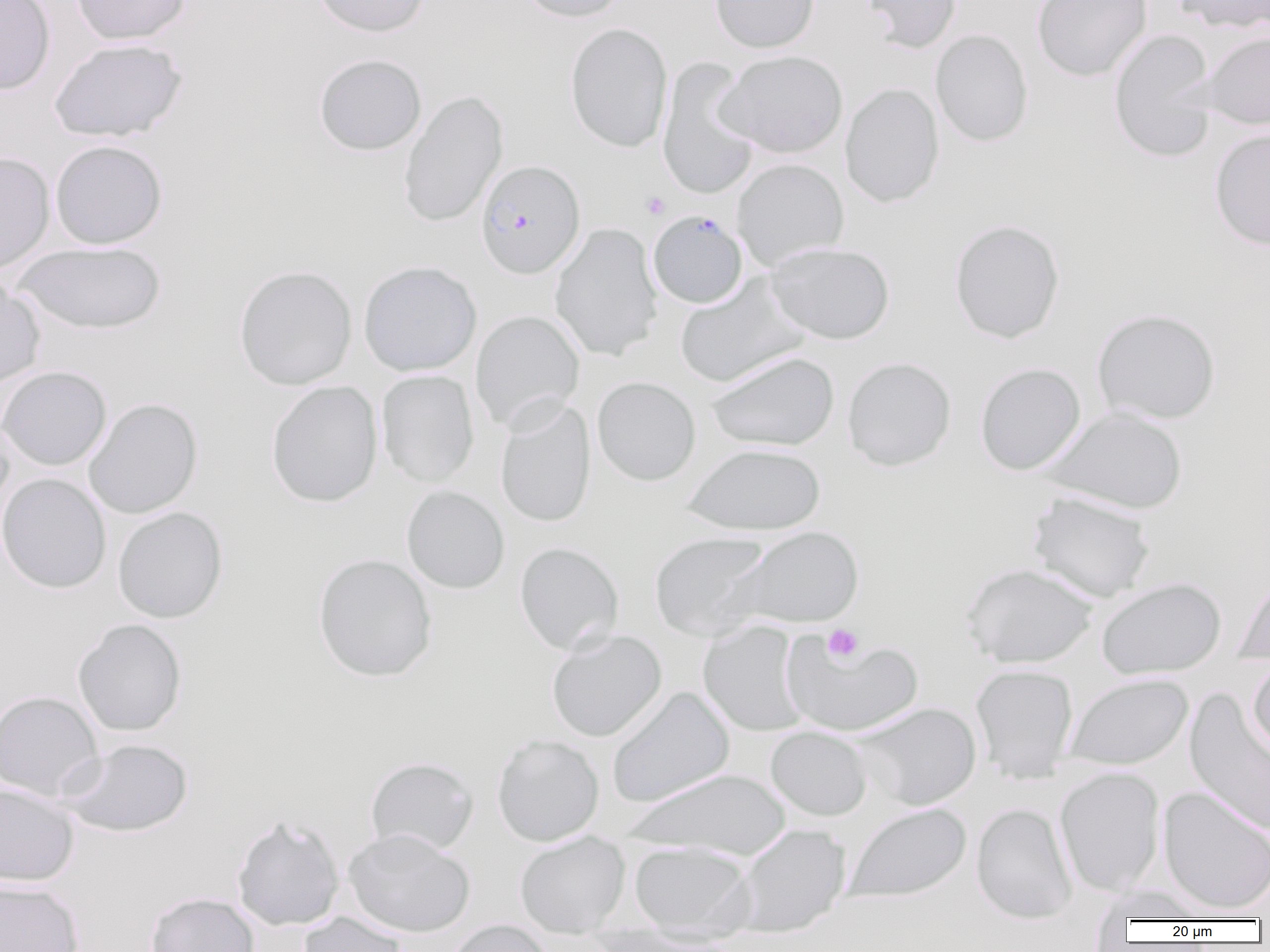
slide-level diagnosis = Plasmodium falciparum
platelet locations = approximate bounding boxes as named x1/y1/x2/y2 corners in pixels: (x1=641, y1=192, x2=670, y2=219), (x1=822, y1=624, x2=864, y2=662)
preparation = thin blood film
Plasmodium falciparum-infected red blood cell locations = approximate bounding boxes as named x1/y1/x2/y2 corners in pixels: (x1=475, y1=159, x2=585, y2=279), (x1=648, y1=210, x2=748, y2=308)
image size = 1270×952 pixels
field of view = one of a larger specimen
magnification = 1000x
modality = optical microscopy
uninfected red blood cell locations = approximate bounding boxes as named x1/y1/x2/y2 corners in pixels: (x1=0, y1=0, x2=56, y2=94), (x1=71, y1=0, x2=191, y2=45), (x1=312, y1=0, x2=430, y2=37), (x1=516, y1=0, x2=629, y2=22), (x1=709, y1=0, x2=820, y2=53), (x1=859, y1=0, x2=963, y2=52), (x1=1032, y1=0, x2=1153, y2=82), (x1=1174, y1=0, x2=1270, y2=34), (x1=564, y1=23, x2=673, y2=153), (x1=930, y1=29, x2=1033, y2=147), (x1=1108, y1=29, x2=1218, y2=163), (x1=1200, y1=31, x2=1270, y2=130), (x1=50, y1=38, x2=187, y2=142), (x1=715, y1=50, x2=848, y2=159), (x1=313, y1=53, x2=427, y2=156), (x1=657, y1=57, x2=761, y2=201), (x1=840, y1=82, x2=944, y2=208), (x1=399, y1=89, x2=508, y2=228), (x1=1209, y1=126, x2=1270, y2=251), (x1=50, y1=139, x2=167, y2=249), (x1=0, y1=151, x2=55, y2=276), (x1=731, y1=158, x2=849, y2=271), (x1=949, y1=218, x2=1065, y2=344), (x1=549, y1=222, x2=663, y2=362), (x1=13, y1=242, x2=166, y2=334), (x1=766, y1=242, x2=895, y2=344), (x1=358, y1=261, x2=482, y2=376), (x1=234, y1=265, x2=357, y2=390), (x1=675, y1=273, x2=809, y2=388), (x1=0, y1=277, x2=45, y2=388), (x1=1091, y1=308, x2=1220, y2=425), (x1=470, y1=309, x2=585, y2=433), (x1=705, y1=351, x2=839, y2=451), (x1=842, y1=356, x2=957, y2=471), (x1=975, y1=362, x2=1086, y2=475), (x1=0, y1=366, x2=112, y2=471), (x1=376, y1=370, x2=479, y2=488), (x1=592, y1=376, x2=701, y2=486), (x1=266, y1=381, x2=383, y2=508), (x1=84, y1=398, x2=203, y2=519), (x1=495, y1=399, x2=596, y2=528), (x1=1043, y1=406, x2=1188, y2=514), (x1=0, y1=415, x2=15, y2=519), (x1=683, y1=443, x2=826, y2=534), (x1=0, y1=473, x2=111, y2=593), (x1=401, y1=485, x2=510, y2=594), (x1=1027, y1=491, x2=1157, y2=603), (x1=113, y1=507, x2=228, y2=623), (x1=727, y1=526, x2=864, y2=629), (x1=649, y1=531, x2=774, y2=641), (x1=514, y1=542, x2=624, y2=655), (x1=312, y1=553, x2=438, y2=682), (x1=961, y1=563, x2=1099, y2=668), (x1=1234, y1=571, x2=1270, y2=665), (x1=1097, y1=578, x2=1226, y2=679), (x1=72, y1=619, x2=187, y2=737), (x1=698, y1=620, x2=810, y2=736), (x1=546, y1=629, x2=667, y2=742), (x1=781, y1=633, x2=923, y2=736), (x1=1247, y1=659, x2=1270, y2=759), (x1=970, y1=664, x2=1079, y2=783), (x1=1064, y1=674, x2=1193, y2=771), (x1=606, y1=686, x2=735, y2=808), (x1=1184, y1=689, x2=1270, y2=836), (x1=0, y1=690, x2=104, y2=801), (x1=855, y1=702, x2=982, y2=810), (x1=765, y1=726, x2=872, y2=820), (x1=492, y1=734, x2=604, y2=846), (x1=60, y1=738, x2=193, y2=837), (x1=365, y1=756, x2=479, y2=855), (x1=1054, y1=767, x2=1166, y2=896), (x1=623, y1=768, x2=793, y2=858), (x1=0, y1=782, x2=79, y2=886), (x1=1157, y1=786, x2=1270, y2=915), (x1=844, y1=802, x2=971, y2=904), (x1=971, y1=802, x2=1078, y2=923), (x1=231, y1=814, x2=345, y2=931), (x1=735, y1=824, x2=851, y2=938), (x1=342, y1=828, x2=475, y2=938), (x1=515, y1=832, x2=630, y2=937), (x1=629, y1=841, x2=757, y2=938), (x1=0, y1=879, x2=84, y2=952), (x1=1090, y1=885, x2=1214, y2=921), (x1=145, y1=892, x2=260, y2=952), (x1=298, y1=911, x2=409, y2=952), (x1=443, y1=919, x2=554, y2=952)